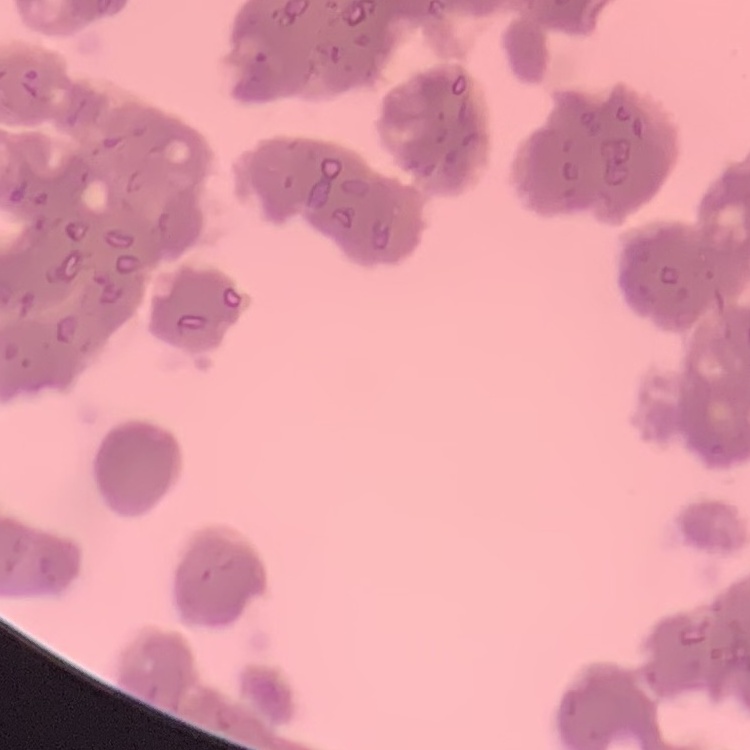
The erythrocytes show rouleaux formation. Thin blood smear. One tile cut from a larger photomicrograph. Stained with either Field's or Giemsa.